Name the blood parasite species.
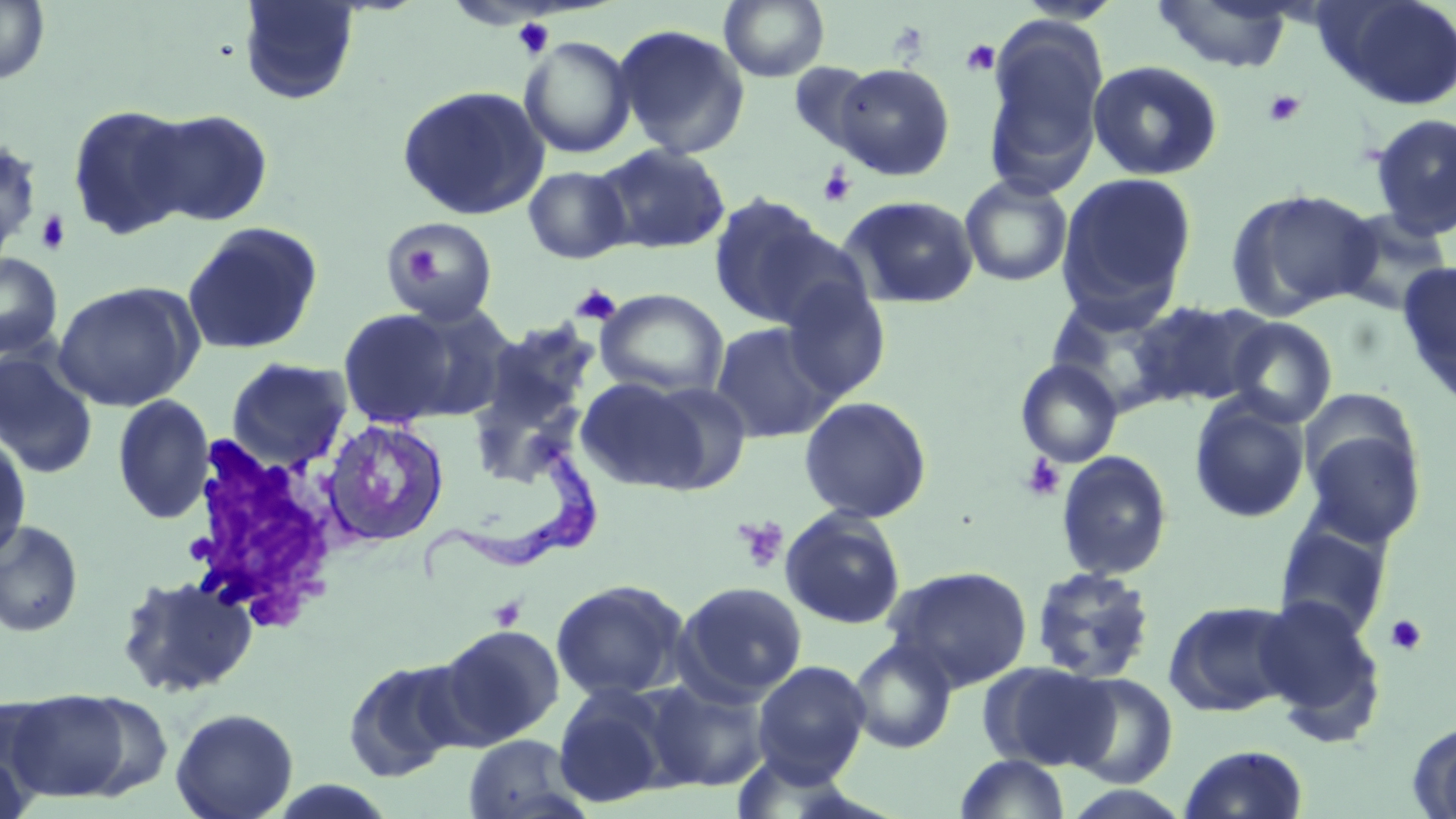
Trypanosoma brucei.

Summary:
  - Coordinate format: approximate bounding boxes as named x1/y1/x2/y2 corners in pixels
  - Trypanosoma brucei locations: (x1=415, y1=448, x2=605, y2=581)
  - Uninfected red blood cell locations: (x1=0, y1=0, x2=51, y2=85), (x1=719, y1=0, x2=829, y2=82), (x1=1315, y1=0, x2=1456, y2=111), (x1=236, y1=1, x2=361, y2=105), (x1=1152, y1=1, x2=1295, y2=73), (x1=983, y1=19, x2=1108, y2=194), (x1=612, y1=23, x2=751, y2=160), (x1=519, y1=36, x2=637, y2=159), (x1=1087, y1=60, x2=1223, y2=181), (x1=788, y1=62, x2=878, y2=155), (x1=833, y1=63, x2=955, y2=181), (x1=396, y1=84, x2=550, y2=221), (x1=67, y1=103, x2=197, y2=239), (x1=140, y1=108, x2=274, y2=226), (x1=1368, y1=112, x2=1456, y2=239), (x1=0, y1=137, x2=43, y2=253), (x1=595, y1=144, x2=732, y2=254), (x1=523, y1=165, x2=632, y2=264), (x1=1057, y1=172, x2=1198, y2=314), (x1=959, y1=175, x2=1074, y2=287), (x1=1225, y1=187, x2=1378, y2=320), (x1=707, y1=192, x2=840, y2=327), (x1=839, y1=195, x2=980, y2=309), (x1=1330, y1=207, x2=1455, y2=317), (x1=386, y1=217, x2=497, y2=326), (x1=181, y1=221, x2=323, y2=355), (x1=749, y1=225, x2=874, y2=331), (x1=0, y1=252, x2=62, y2=359), (x1=1397, y1=262, x2=1456, y2=403), (x1=53, y1=281, x2=202, y2=411), (x1=780, y1=283, x2=891, y2=402), (x1=593, y1=288, x2=729, y2=398), (x1=1046, y1=296, x2=1179, y2=415), (x1=1129, y1=299, x2=1274, y2=408), (x1=396, y1=301, x2=518, y2=423), (x1=337, y1=308, x2=464, y2=428), (x1=472, y1=315, x2=603, y2=453), (x1=1224, y1=316, x2=1338, y2=428), (x1=710, y1=321, x2=840, y2=443), (x1=0, y1=348, x2=99, y2=480), (x1=225, y1=357, x2=354, y2=471), (x1=1015, y1=359, x2=1123, y2=468), (x1=574, y1=376, x2=712, y2=492), (x1=636, y1=380, x2=753, y2=493), (x1=112, y1=395, x2=215, y2=524), (x1=799, y1=396, x2=933, y2=524), (x1=1189, y1=396, x2=1311, y2=524), (x1=321, y1=418, x2=450, y2=548), (x1=1302, y1=427, x2=1427, y2=548), (x1=0, y1=432, x2=33, y2=564), (x1=1055, y1=450, x2=1174, y2=581), (x1=780, y1=508, x2=906, y2=631), (x1=0, y1=520, x2=84, y2=638), (x1=1273, y1=522, x2=1392, y2=640), (x1=885, y1=566, x2=1033, y2=691), (x1=1030, y1=567, x2=1157, y2=684), (x1=115, y1=573, x2=259, y2=699), (x1=550, y1=580, x2=689, y2=702), (x1=675, y1=581, x2=807, y2=703), (x1=1253, y1=594, x2=1386, y2=734), (x1=1164, y1=600, x2=1299, y2=718), (x1=434, y1=624, x2=565, y2=747), (x1=848, y1=638, x2=958, y2=754), (x1=342, y1=657, x2=469, y2=784), (x1=752, y1=660, x2=872, y2=782), (x1=984, y1=663, x2=1120, y2=772), (x1=1062, y1=673, x2=1178, y2=788), (x1=646, y1=678, x2=771, y2=791), (x1=553, y1=684, x2=675, y2=808), (x1=5, y1=689, x2=139, y2=803), (x1=170, y1=707, x2=299, y2=819), (x1=1409, y1=721, x2=1456, y2=818), (x1=461, y1=733, x2=589, y2=819), (x1=0, y1=742, x2=35, y2=819), (x1=1178, y1=744, x2=1308, y2=819), (x1=955, y1=753, x2=1070, y2=818), (x1=1058, y1=785, x2=1196, y2=819)
  - Platelet locations: (x1=512, y1=17, x2=555, y2=59), (x1=960, y1=40, x2=1001, y2=77), (x1=1263, y1=89, x2=1306, y2=128), (x1=817, y1=165, x2=857, y2=208), (x1=35, y1=211, x2=72, y2=255), (x1=402, y1=245, x2=444, y2=288), (x1=571, y1=284, x2=621, y2=325), (x1=1019, y1=454, x2=1065, y2=502), (x1=733, y1=516, x2=790, y2=574), (x1=489, y1=596, x2=526, y2=631), (x1=1385, y1=615, x2=1427, y2=657)
  - White blood cell locations: (x1=180, y1=436, x2=353, y2=629)
  - Modality: light microscopy
  - Magnification: 1000x
  - Field of view: one of a larger specimen
  - Preparation: thin blood smear
  - Image size: 1456×819 pixels
  - Stain: May-Grünwald-Giemsa